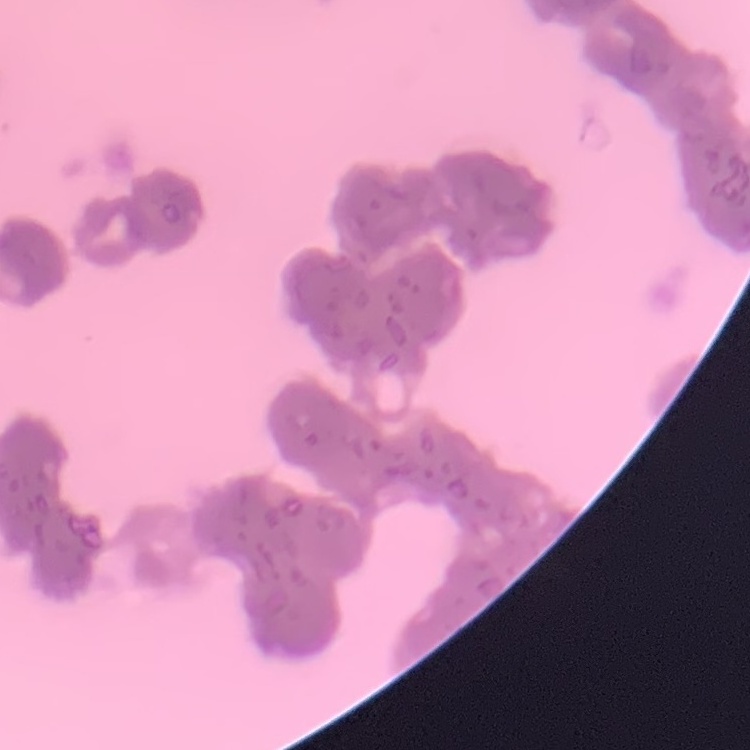

erythrocyte morphology = rouleaux formation
image type = one tile cut from a larger photomicrograph
stain = Field's or Giemsa
preparation = thin blood film